Outline each uninfected red blood cell.
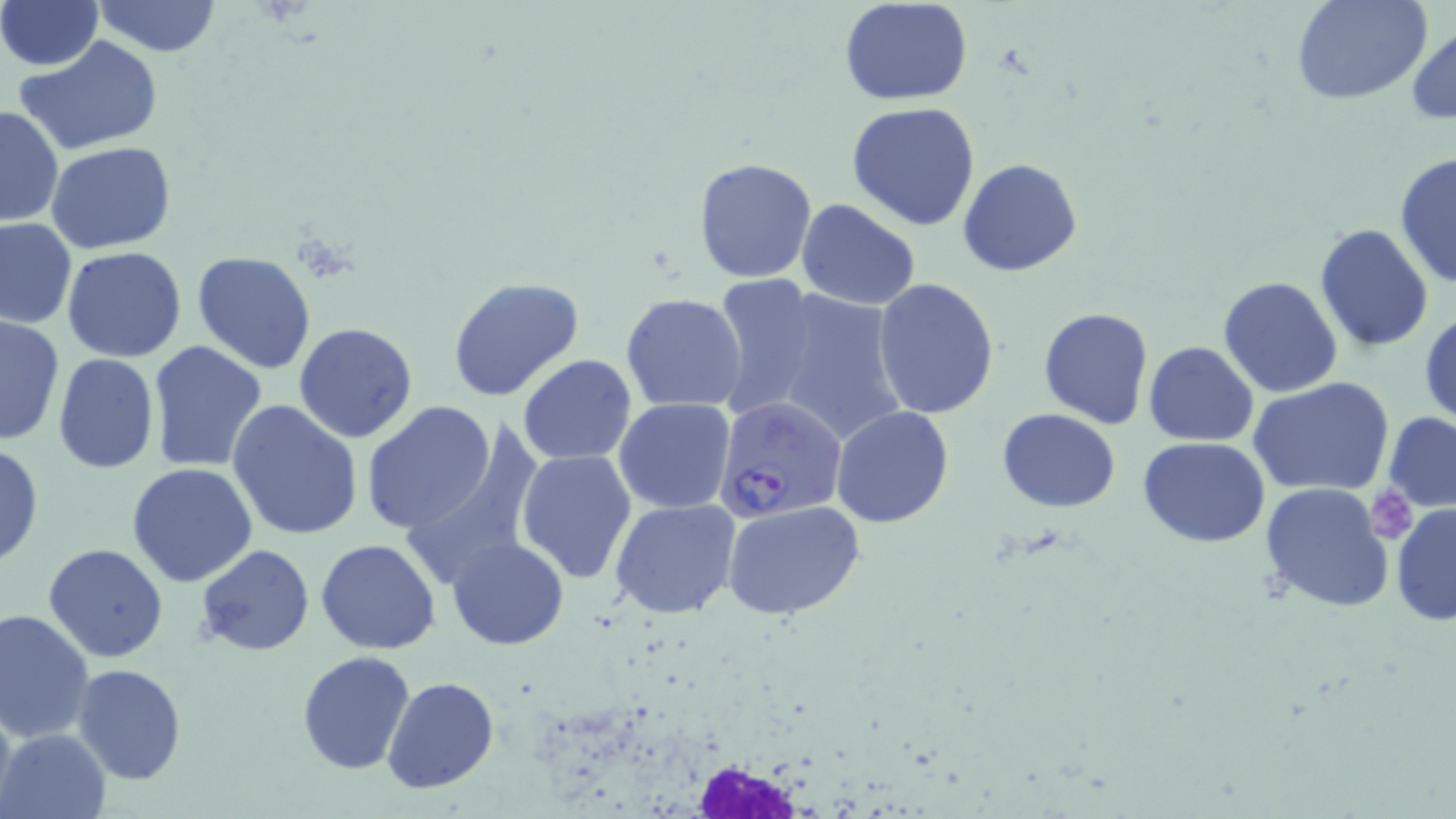

Approximate bounding boxes as (x1,y1)-(x2,y2) corner pairs in pixels.
Uninfected red blood cells: (92,0)-(221,57), (839,0)-(974,105), (1293,0)-(1432,105), (0,1)-(102,71), (1407,22)-(1456,125), (15,36)-(164,157), (847,101)-(982,232), (0,104)-(64,228), (47,141)-(177,254), (1394,153)-(1455,289), (692,156)-(817,282), (959,158)-(1083,277), (797,199)-(922,310), (0,218)-(78,328), (1314,224)-(1435,352), (61,246)-(188,363), (190,251)-(317,375), (707,274)-(823,418), (1218,275)-(1343,397), (446,276)-(586,403), (873,277)-(998,418), (756,284)-(909,449), (622,293)-(748,410), (1039,306)-(1154,427), (1419,308)-(1455,431), (1,314)-(63,449), (293,321)-(417,443), (147,340)-(267,472), (1144,341)-(1259,446), (53,353)-(160,475), (518,355)-(636,463), (1248,377)-(1396,497), (614,399)-(737,514), (228,400)-(364,541), (360,402)-(498,536), (831,407)-(956,528), (996,408)-(1123,511), (1383,411)-(1456,512), (1139,437)-(1271,547), (0,441)-(43,569), (516,448)-(637,582), (127,462)-(259,588), (1259,481)-(1396,612), (609,498)-(741,618), (719,499)-(869,623), (1391,503)-(1456,628), (315,538)-(439,654), (446,538)-(570,650), (42,544)-(168,664), (195,545)-(314,657), (0,607)-(96,742), (296,651)-(416,773), (72,665)-(189,785), (383,676)-(499,794), (0,690)-(17,818), (2,728)-(109,817).

White blood cell locations: (638,733)-(853,814). Plasmodium falciparum-infected red blood cell locations: (713,396)-(847,524). Platelet locations: (1366,492)-(1419,544). Slide-level diagnosis: Plasmodium falciparum. Light microscopy. Captured at 1000x magnification. May-Grünwald-Giemsa stain. Image is 1456×819 pixels. Thin blood smear. Single field of view.